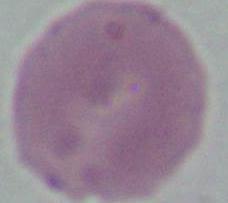

Summary:
  - Identification: red blood cell
  - Modality: micrograph
  - Magnification: 1000x